Report the malaria status of this cell.
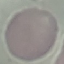

Uninfected.

capture = smartphone camera at the microscope eyepiece
image type = cell patch, automatically extracted from a larger field of view and resized to 64 × 64 pixels
preparation = thin blood film
stain = Giemsa